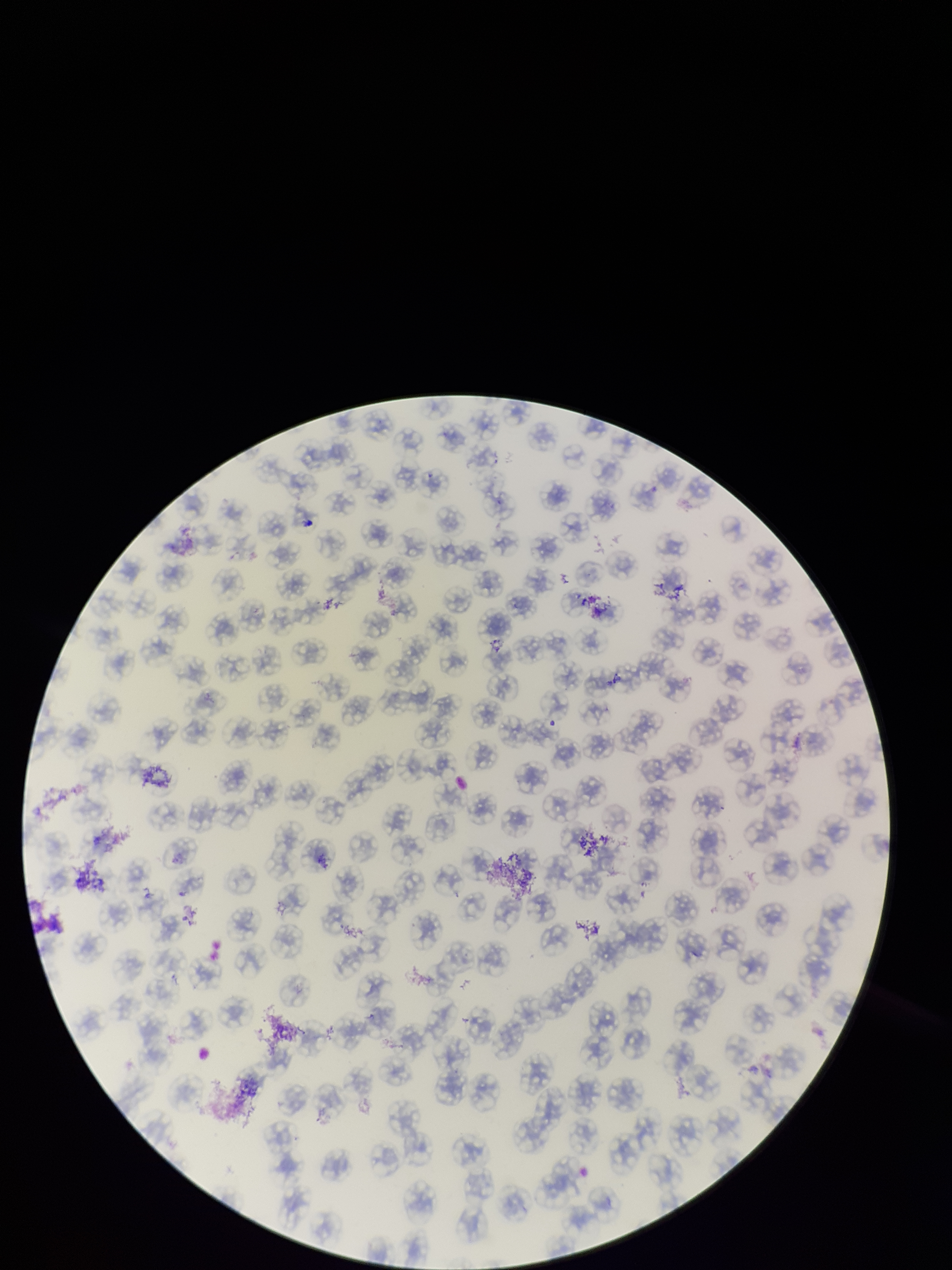 Parasitized red blood cell count: 0. Patient malaria status: negative. Smartphone photograph taken through the eyepiece of a microscope. Red blood cell count: 144. Preparation: thin blood smear. Parasitized red blood cells: none identified. One field from this slide. Image is 952×1270 pixels. Giemsa stain.